Describe the morphology of the erythrocytes.
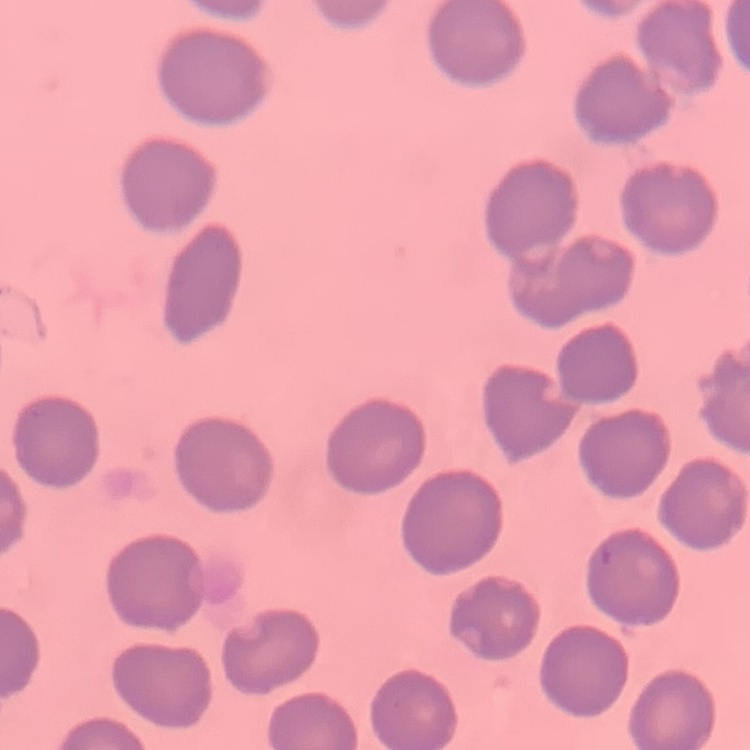
They show no rouleaux formation.

Summary:
  - Image type: one tile cut from a larger photomicrograph
  - Preparation: thin blood film
  - Stain: Field's or Giemsa